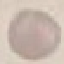
{
  "result": "no malaria parasites seen",
  "image_type": "cell patch, automatically extracted from a larger field of view and resized to 64 × 64 pixels",
  "stain": "Giemsa",
  "capture": "smartphone camera at the microscope eyepiece",
  "preparation": "thin blood smear"
}